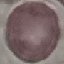

Malaria status: uninfected. Thin blood film. Photographed with a smartphone camera at the microscope eyepiece. Giemsa stain. Automatically extracted cell patch, resized to 64 × 64 pixels.